Locate and identify every blood parasite.
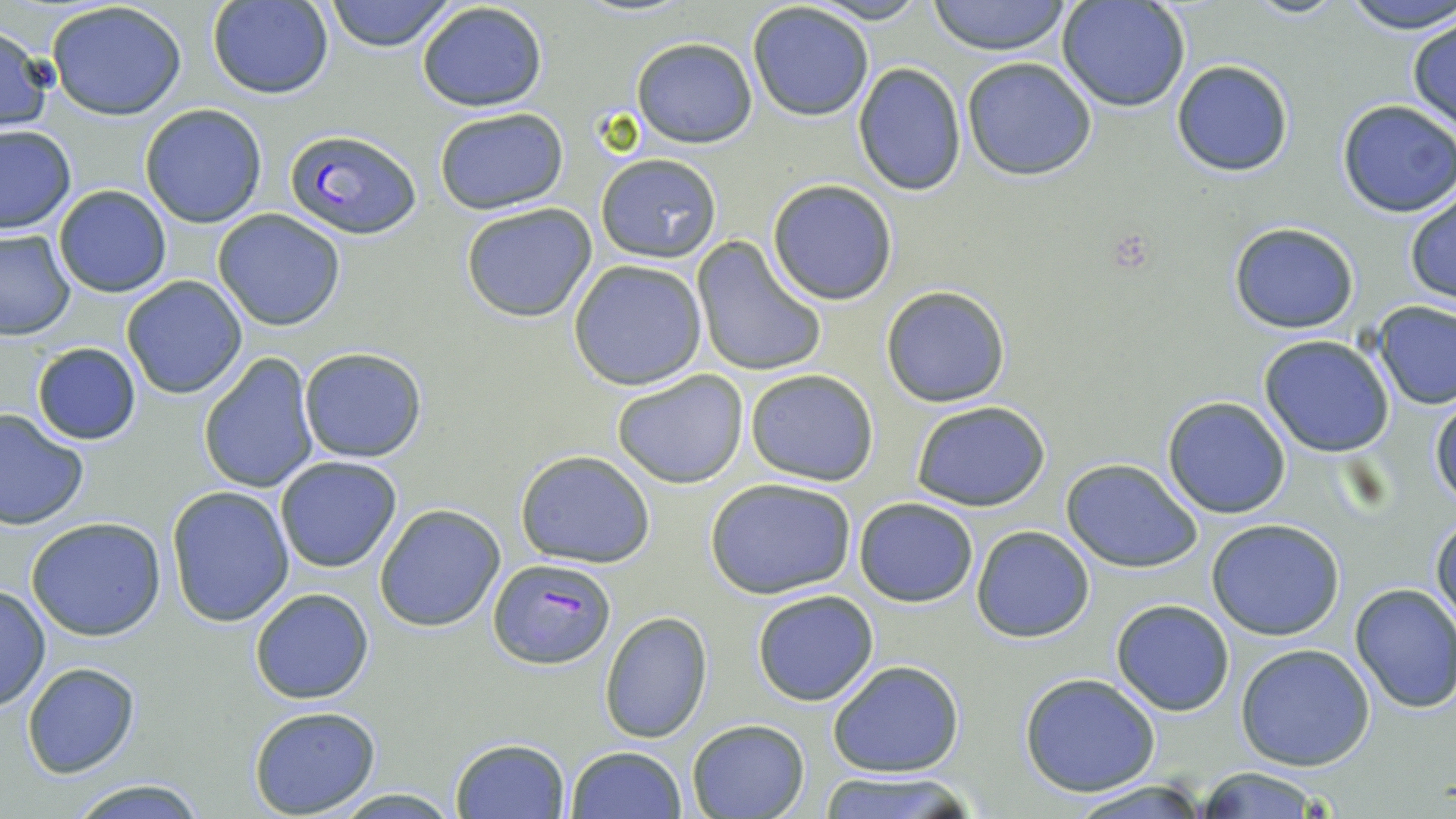
Approximate bounding boxes as (x1,y1)-(x2,y2) corner pairs in pixels.
Plasmodium falciparum-infected red blood cells: (285,127)-(422,239), (486,558)-(616,668).
No Plasmodium ovale, Plasmodium malariae, Plasmodium vivax, Babesia divergens, or Trypanosoma brucei observed.

slide-level diagnosis = Plasmodium falciparum
stain = May-Grünwald-Giemsa
preparation = thin blood film
uninfected red blood cell locations = approximate bounding boxes as (x1,y1)-(x2,y2) corner pairs in pixels: (323,0)-(457,51), (803,0)-(933,25), (927,0)-(1074,56), (1056,0)-(1192,113), (1242,0)-(1350,18), (1343,0)-(1456,35), (46,1)-(188,120), (208,1)-(333,100), (415,2)-(549,114), (747,3)-(873,120), (1406,15)-(1455,132), (0,25)-(55,132), (630,37)-(758,149), (960,57)-(1099,181), (1172,60)-(1294,177), (851,63)-(968,197), (1336,99)-(1456,217), (140,104)-(269,228), (433,107)-(569,214), (0,126)-(75,234), (595,154)-(723,263), (767,180)-(898,304), (53,185)-(172,298), (1404,193)-(1455,306), (460,203)-(597,322), (212,209)-(347,330), (1227,222)-(1359,333), (0,229)-(75,339), (691,238)-(827,378), (568,259)-(708,390), (120,275)-(247,399), (881,285)-(1011,407), (1372,301)-(1456,411), (1259,335)-(1395,458), (31,342)-(142,445), (297,347)-(428,463), (198,352)-(319,494), (611,368)-(749,490), (744,369)-(880,484), (1429,393)-(1455,510), (1162,397)-(1292,519), (911,400)-(1053,512), (0,409)-(90,530), (515,450)-(656,568), (274,456)-(402,573), (1062,459)-(1204,573), (705,477)-(856,599), (166,485)-(295,626), (854,497)-(979,606), (374,503)-(505,632), (1430,515)-(1455,630), (25,517)-(168,641), (1206,519)-(1345,641), (972,526)-(1094,642), (1349,583)-(1456,713), (0,584)-(51,711), (250,588)-(375,705), (752,589)-(880,706), (1111,600)-(1235,716), (598,610)-(715,743), (1237,643)-(1375,771), (828,659)-(965,779), (21,662)-(140,778), (1018,672)-(1160,797), (247,706)-(382,816), (687,718)-(808,819), (449,737)-(571,819), (566,745)-(686,819), (1187,768)-(1332,818), (816,771)-(977,819), (65,776)-(210,817), (1063,780)-(1215,818), (324,788)-(467,818)
image size = 1456×819 pixels
field of view = single
magnification = 1000x
modality = optical microscopy